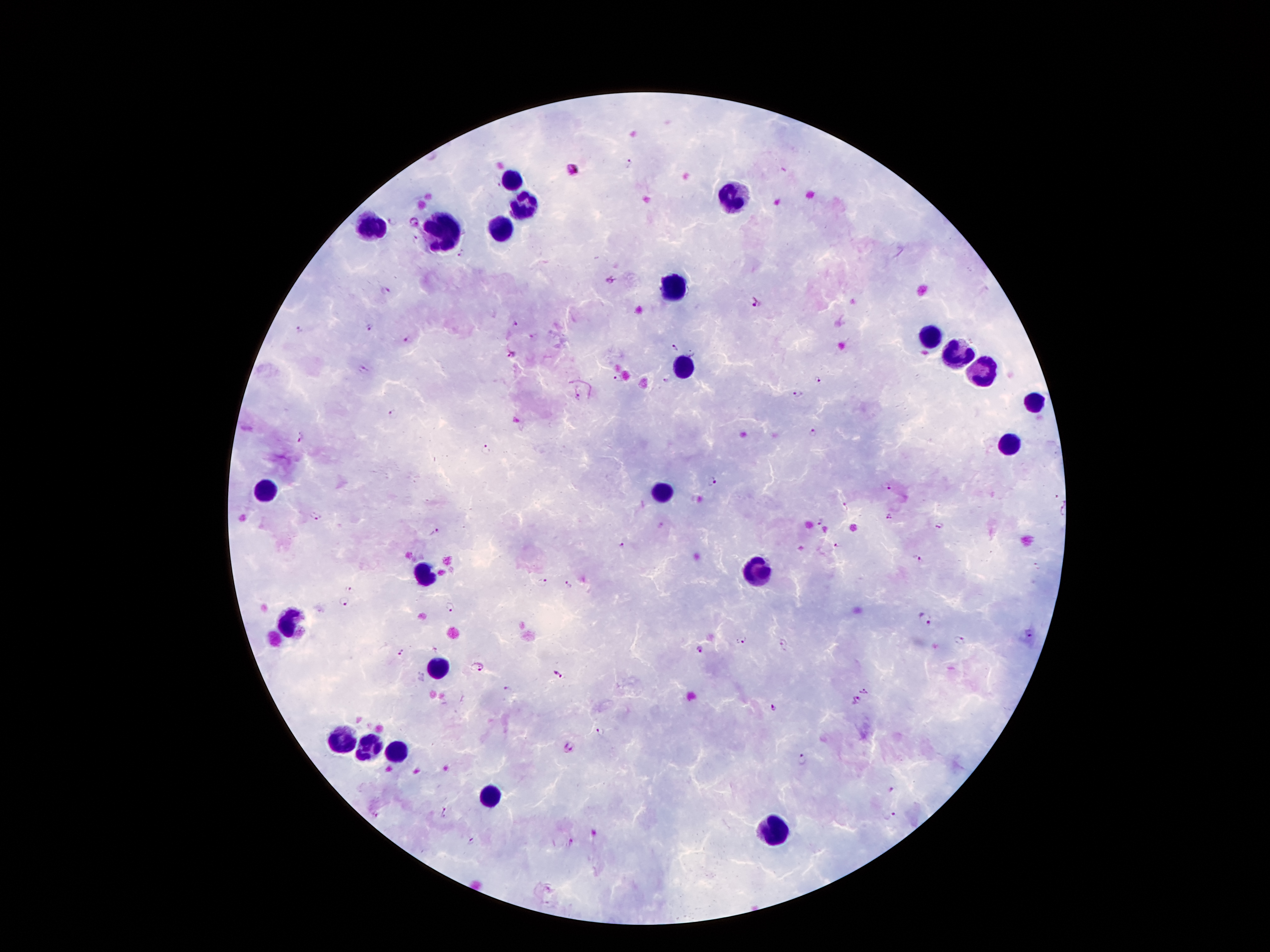
Approximate object centers, in pixels from the top-left corner.
Summary:
  - Malaria parasite locations: (x=629, y=161), (x=572, y=170), (x=391, y=220), (x=414, y=222), (x=612, y=281), (x=384, y=291), (x=755, y=303), (x=515, y=324), (x=371, y=325), (x=300, y=331), (x=408, y=339), (x=675, y=347), (x=513, y=354), (x=363, y=370), (x=618, y=378), (x=664, y=379), (x=818, y=380), (x=797, y=392), (x=578, y=398), (x=392, y=413), (x=813, y=432), (x=300, y=437), (x=485, y=449), (x=712, y=482), (x=887, y=487), (x=846, y=505), (x=316, y=516), (x=889, y=517), (x=820, y=521), (x=940, y=526), (x=434, y=532), (x=839, y=544), (x=622, y=546), (x=921, y=561), (x=1037, y=566), (x=543, y=584), (x=569, y=585), (x=351, y=590), (x=342, y=603), (x=451, y=606), (x=925, y=619), (x=743, y=641), (x=959, y=641), (x=784, y=644), (x=700, y=648), (x=436, y=650), (x=400, y=652), (x=479, y=665), (x=557, y=673), (x=506, y=689), (x=864, y=692), (x=856, y=701), (x=773, y=708), (x=601, y=733), (x=568, y=748), (x=802, y=759), (x=892, y=789), (x=443, y=812), (x=374, y=814), (x=893, y=814), (x=572, y=841), (x=470, y=842)
  - Leukocyte locations: (x=510, y=179), (x=732, y=195), (x=523, y=202), (x=371, y=227), (x=502, y=229), (x=445, y=231), (x=676, y=286), (x=930, y=338), (x=957, y=351), (x=684, y=367), (x=984, y=368), (x=1033, y=405), (x=1010, y=447), (x=267, y=487), (x=661, y=493), (x=756, y=567), (x=424, y=573), (x=288, y=622), (x=435, y=666), (x=340, y=741), (x=367, y=750), (x=397, y=750), (x=489, y=794), (x=772, y=830)
  - Stain: Giemsa
  - Capture: smartphone camera through the microscope eyepiece
  - Patient malaria status: infected with Plasmodium falciparum
  - Preparation: thick blood smear
  - Magnification: 100x
  - Field of view: one from this slide
  - Image size: 1270×952 pixels